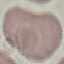

{
  "result": "no malaria parasites seen",
  "preparation": "thin blood smear",
  "capture": "smartphone camera at the microscope eyepiece",
  "stain": "Giemsa",
  "image_type": "automatically extracted cell patch, resized to 64 × 64 pixels"
}